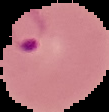
result = malaria parasites detected
image type = segmented cell region on a black background
image size = 109×112 pixels
preparation = thin blood film